Assess this cell for malaria.
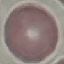
Uninfected.

{
  "image_type": "automatically extracted cell patch, resized to 64 × 64 pixels",
  "preparation": "thin blood film",
  "capture": "smartphone through the microscope eyepiece",
  "stain": "Giemsa"
}